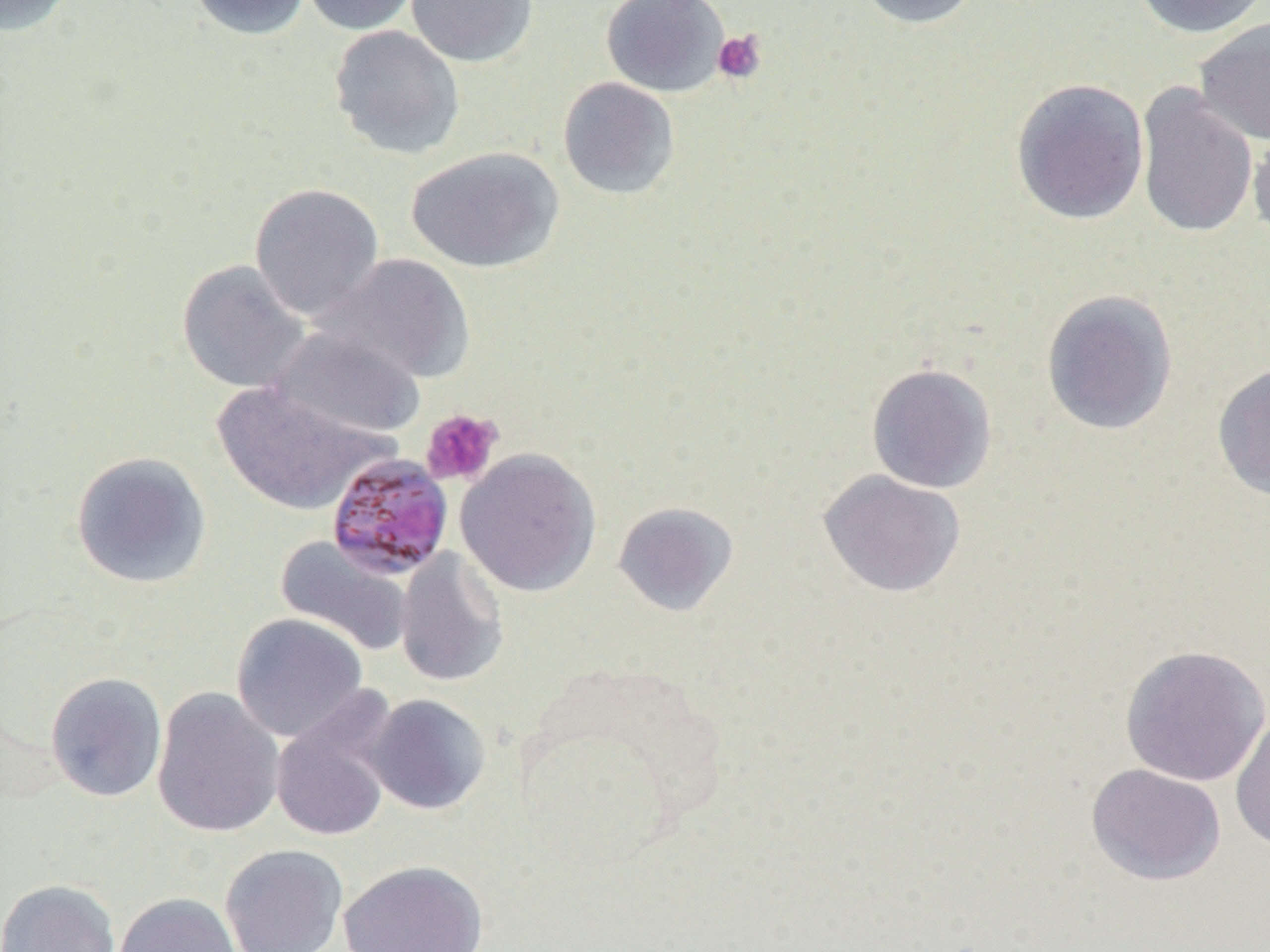

slide-level diagnosis = Plasmodium malariae
uninfected red blood cell locations = approximate bounding boxes as (x1,y1)-(x2,y2) corner pairs in pixels: (0,0)-(77,37), (187,0)-(312,40), (298,0)-(422,35), (406,0)-(538,67), (601,0)-(729,98), (854,0)-(984,29), (1131,0)-(1268,39), (1193,16)-(1270,146), (329,24)-(466,160), (558,76)-(680,200), (1010,77)-(1150,225), (1135,82)-(1258,240), (1247,120)-(1270,244), (405,146)-(564,273), (249,182)-(385,321), (315,253)-(476,385), (176,260)-(312,394), (1041,288)-(1179,436), (268,327)-(427,442), (866,362)-(998,494), (1211,362)-(1270,501), (211,381)-(390,516), (455,448)-(602,597), (70,451)-(212,589), (817,469)-(967,598), (612,501)-(740,617), (274,535)-(415,657), (395,547)-(509,688), (231,613)-(369,742), (1119,644)-(1270,787), (45,671)-(168,802), (151,687)-(285,838), (268,693)-(400,844), (364,693)-(491,815), (1230,712)-(1270,855), (1085,763)-(1226,886), (219,844)-(349,952), (338,859)-(489,952), (0,878)-(122,952), (113,892)-(242,952)
preparation = thin blood film
Plasmodium malariae-infected red blood cell locations = approximate bounding boxes as (x1,y1)-(x2,y2) corner pairs in pixels: (325,452)-(454,580)
modality = optical microscopy
platelet locations = approximate bounding boxes as (x1,y1)-(x2,y2) corner pairs in pixels: (712,30)-(767,84), (420,408)-(503,486)
field of view = one of a larger specimen
image size = 1270×952 pixels
magnification = 1000x